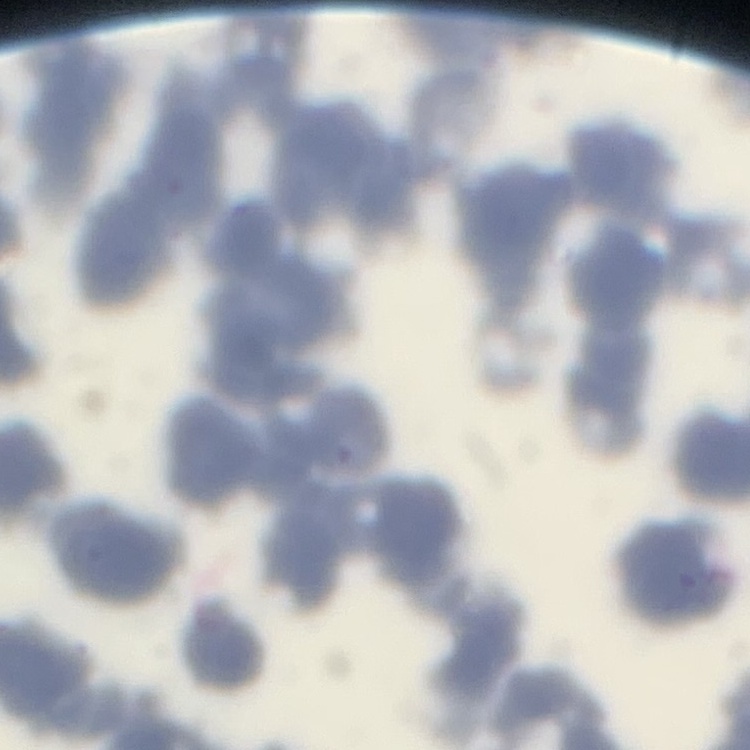
{
  "erythrocyte_morphology": "rouleaux formation",
  "preparation": "thin blood film",
  "stain": "Field's or Giemsa",
  "image_type": "one tile cut from a larger photomicrograph"
}